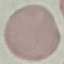

result: no malaria parasites detected
stain: Giemsa
image_type: cell patch, automatically extracted from a larger field of view and resized to 64 × 64 pixels
capture: smartphone camera at the microscope eyepiece
preparation: thin blood smear